Locate and identify every blood parasite.
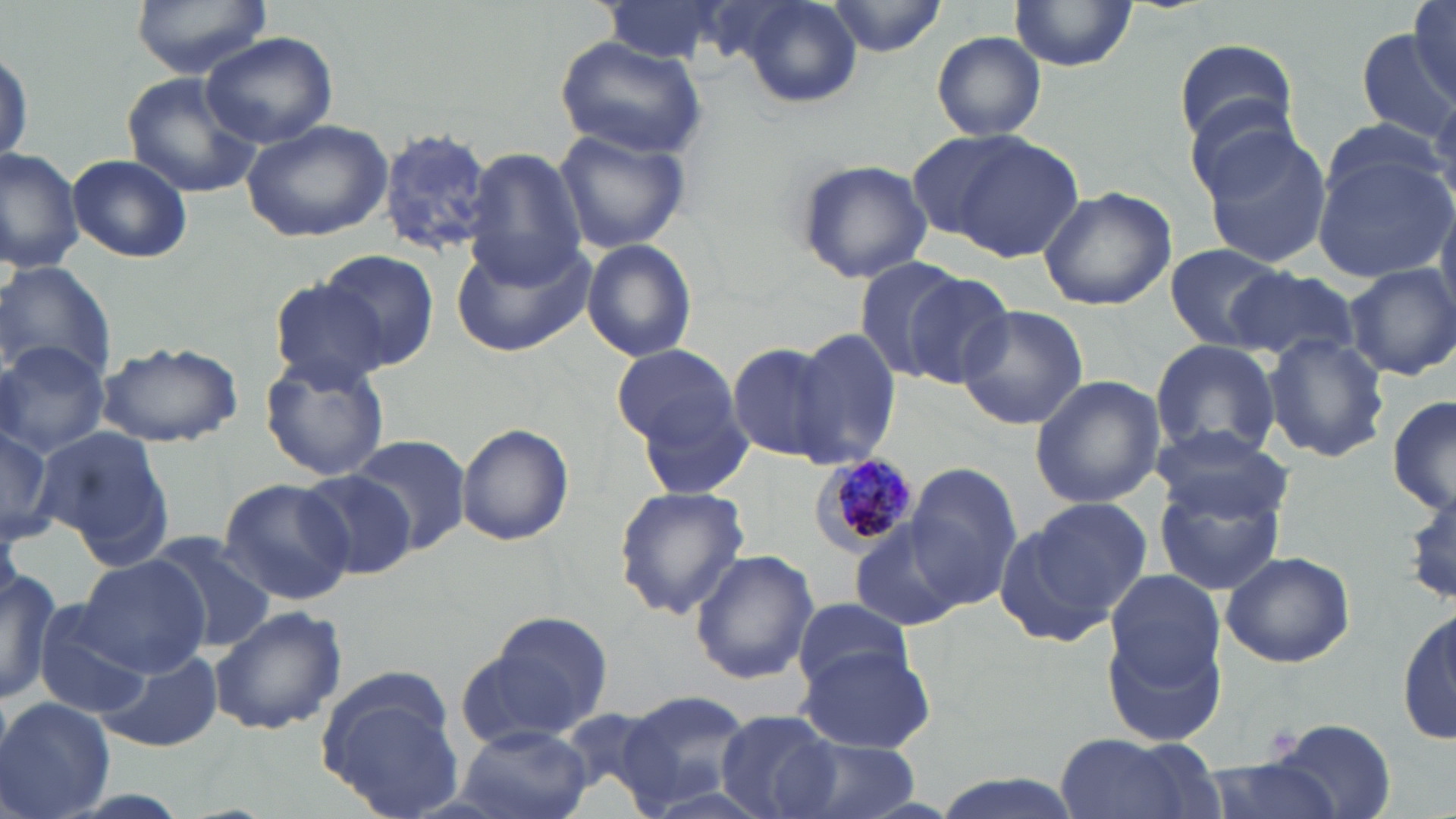

Approximate bounding boxes as named x1/y1/x2/y2 corners in pixels.
Plasmodium malariae-infected red blood cells: (x1=814, y1=455, x2=919, y2=553).
No Plasmodium falciparum, Plasmodium ovale, Plasmodium vivax, Babesia divergens, or Trypanosoma brucei observed.

slide-level diagnosis = Plasmodium malariae
field of view = single
image size = 1456×819 pixels
uninfected red blood cell locations = approximate bounding boxes as named x1/y1/x2/y2 corners in pixels: (x1=129, y1=0, x2=272, y2=77), (x1=599, y1=0, x2=726, y2=67), (x1=825, y1=0, x2=950, y2=53), (x1=1411, y1=0, x2=1456, y2=99), (x1=725, y1=1, x2=864, y2=110), (x1=1009, y1=1, x2=1137, y2=71), (x1=1354, y1=26, x2=1454, y2=152), (x1=200, y1=31, x2=338, y2=149), (x1=930, y1=31, x2=1048, y2=142), (x1=554, y1=34, x2=705, y2=158), (x1=1172, y1=39, x2=1302, y2=148), (x1=124, y1=74, x2=260, y2=197), (x1=1180, y1=86, x2=1309, y2=200), (x1=1319, y1=114, x2=1450, y2=220), (x1=241, y1=118, x2=393, y2=242), (x1=552, y1=124, x2=695, y2=254), (x1=1198, y1=124, x2=1334, y2=270), (x1=377, y1=126, x2=497, y2=258), (x1=946, y1=135, x2=1085, y2=261), (x1=0, y1=147, x2=85, y2=273), (x1=462, y1=148, x2=589, y2=289), (x1=1313, y1=151, x2=1454, y2=283), (x1=67, y1=154, x2=191, y2=263), (x1=795, y1=158, x2=931, y2=284), (x1=1038, y1=186, x2=1175, y2=313), (x1=1436, y1=192, x2=1456, y2=316), (x1=451, y1=233, x2=592, y2=357), (x1=583, y1=240, x2=698, y2=362), (x1=1164, y1=244, x2=1293, y2=351), (x1=312, y1=249, x2=438, y2=372), (x1=853, y1=255, x2=971, y2=381), (x1=0, y1=260, x2=116, y2=388), (x1=1343, y1=263, x2=1456, y2=382), (x1=1223, y1=266, x2=1359, y2=362), (x1=897, y1=269, x2=1019, y2=389), (x1=268, y1=279, x2=393, y2=388), (x1=956, y1=305, x2=1090, y2=430), (x1=793, y1=327, x2=904, y2=466), (x1=1263, y1=334, x2=1389, y2=463), (x1=1150, y1=338, x2=1281, y2=466), (x1=0, y1=340, x2=110, y2=454), (x1=726, y1=341, x2=844, y2=464), (x1=99, y1=342, x2=244, y2=447), (x1=612, y1=343, x2=740, y2=451), (x1=259, y1=354, x2=390, y2=481), (x1=1030, y1=375, x2=1167, y2=508), (x1=628, y1=381, x2=757, y2=502), (x1=1388, y1=393, x2=1456, y2=519), (x1=0, y1=421, x2=64, y2=543), (x1=455, y1=422, x2=574, y2=545), (x1=1154, y1=423, x2=1287, y2=524), (x1=36, y1=427, x2=172, y2=566), (x1=347, y1=433, x2=472, y2=556), (x1=905, y1=464, x2=1021, y2=609), (x1=295, y1=469, x2=417, y2=580), (x1=1153, y1=471, x2=1288, y2=597), (x1=218, y1=478, x2=355, y2=605), (x1=612, y1=486, x2=751, y2=619), (x1=997, y1=505, x2=1149, y2=642), (x1=850, y1=523, x2=965, y2=632), (x1=143, y1=535, x2=277, y2=655), (x1=689, y1=549, x2=819, y2=685), (x1=1219, y1=550, x2=1355, y2=668), (x1=75, y1=554, x2=211, y2=678), (x1=0, y1=562, x2=60, y2=708), (x1=1101, y1=574, x2=1227, y2=744), (x1=1398, y1=598, x2=1456, y2=752), (x1=792, y1=599, x2=915, y2=692), (x1=32, y1=602, x2=157, y2=721), (x1=209, y1=606, x2=347, y2=736), (x1=462, y1=619, x2=610, y2=748), (x1=91, y1=645, x2=223, y2=753), (x1=797, y1=646, x2=938, y2=753), (x1=316, y1=681, x2=466, y2=819), (x1=614, y1=688, x2=755, y2=815), (x1=0, y1=697, x2=115, y2=819), (x1=715, y1=709, x2=841, y2=819), (x1=1263, y1=716, x2=1398, y2=815), (x1=455, y1=728, x2=594, y2=819), (x1=1051, y1=733, x2=1220, y2=819), (x1=785, y1=736, x2=926, y2=819), (x1=1193, y1=759, x2=1343, y2=819)
stain = May-Grünwald-Giemsa
preparation = thin blood smear
magnification = 1000x
modality = optical microscopy